Identify the parasite.
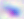
This is Toxoplasma gondii.

400x magnification. Photomicrograph.